Assess the morphology of the red blood cells.
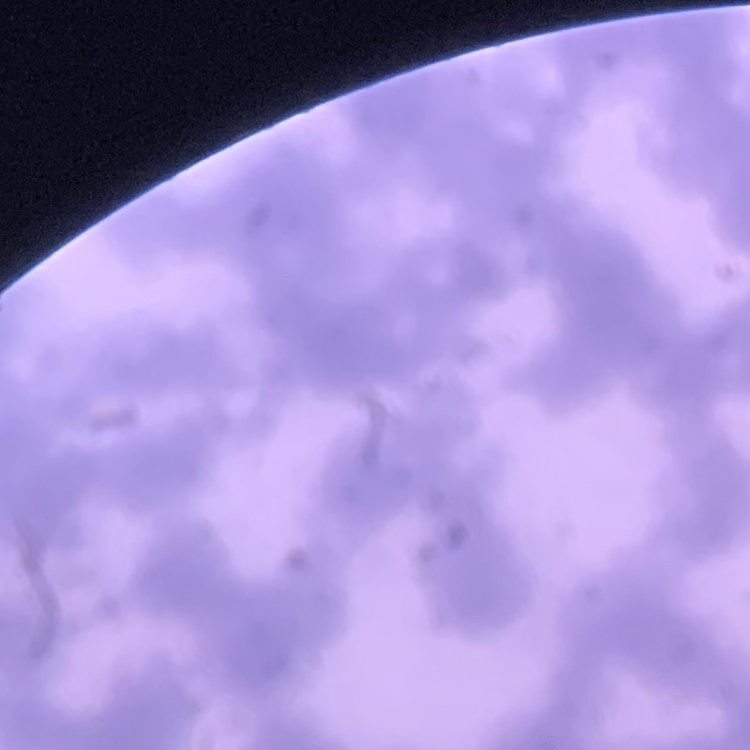

They show rouleaux formation.

Thin blood film. Field's or Giemsa stain. Square crop of a larger photomicrograph.